Assess the morphology of the red blood cells.
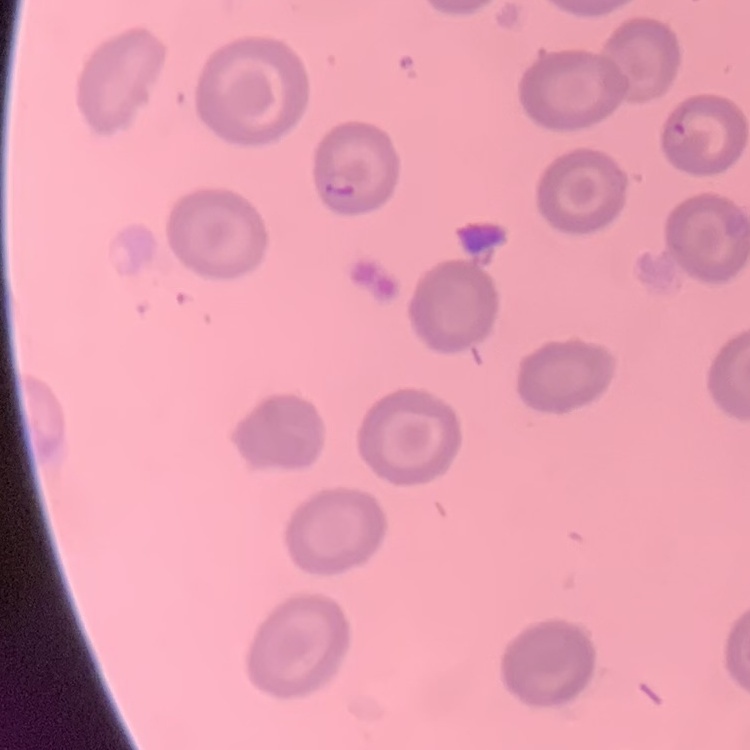

They show no rouleaux formation.

preparation: thin peripheral smear
stain: Field's or Giemsa
image_type: square crop of a larger photomicrograph